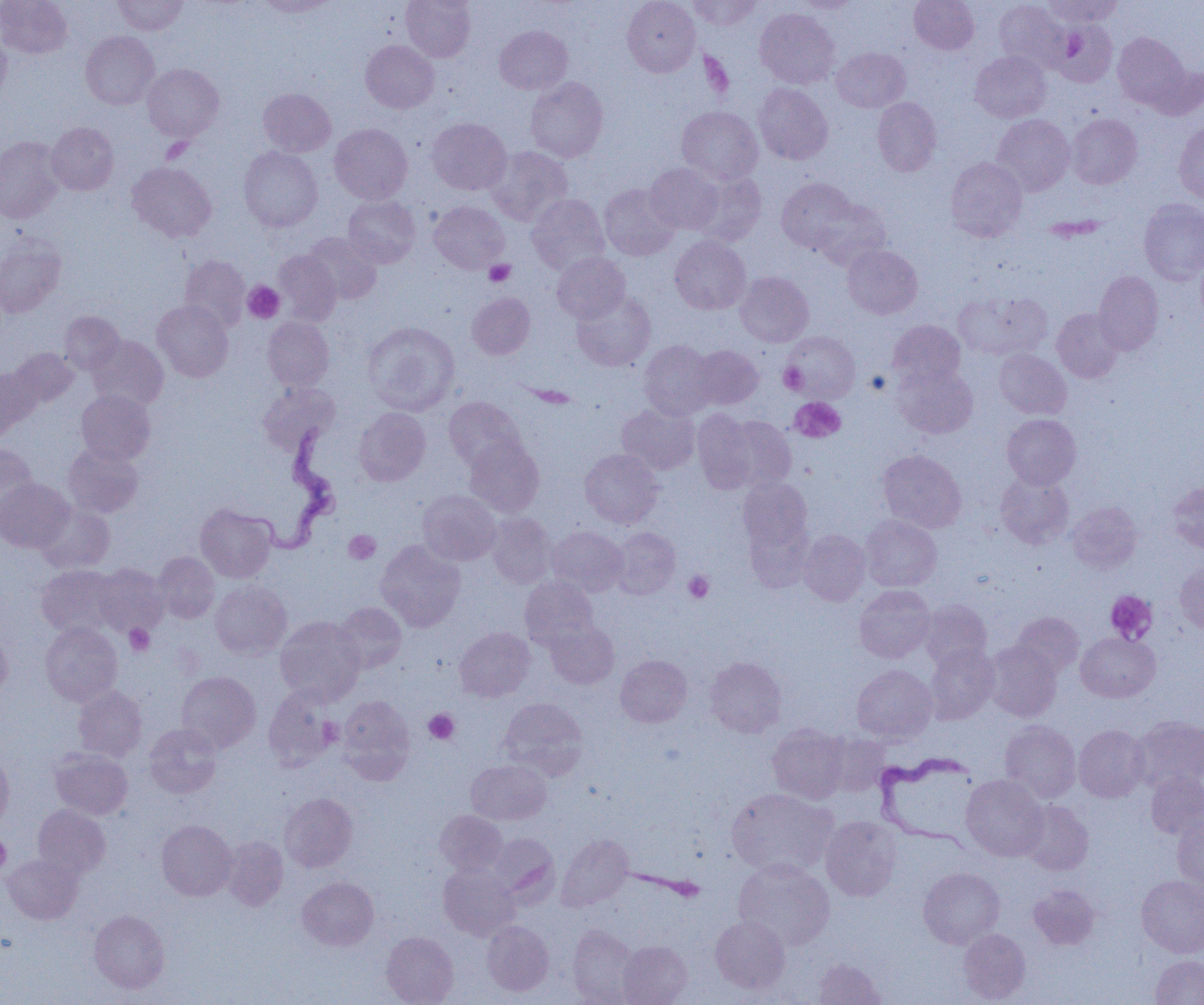

Summary:
  - Coordinate format: approximate bounding boxes as named x1/y1/x2/y2 corners in pixels
  - Trypanosoma brucei locations: (x1=244, y1=421, x2=342, y2=554), (x1=875, y1=750, x2=978, y2=850)
  - Platelet locations: (x1=161, y1=137, x2=192, y2=163), (x1=485, y1=259, x2=515, y2=286), (x1=243, y1=281, x2=284, y2=323), (x1=779, y1=363, x2=807, y2=394), (x1=865, y1=370, x2=890, y2=395), (x1=790, y1=397, x2=845, y2=442), (x1=344, y1=530, x2=381, y2=564), (x1=684, y1=571, x2=714, y2=603), (x1=1105, y1=590, x2=1157, y2=643), (x1=124, y1=624, x2=155, y2=655), (x1=424, y1=709, x2=459, y2=744), (x1=318, y1=717, x2=344, y2=746), (x1=0, y1=835, x2=10, y2=875)
  - Uninfected red blood cell locations: (x1=0, y1=0, x2=71, y2=58), (x1=112, y1=0, x2=188, y2=35), (x1=254, y1=0, x2=337, y2=17), (x1=401, y1=0, x2=475, y2=61), (x1=622, y1=0, x2=700, y2=76), (x1=687, y1=0, x2=762, y2=30), (x1=909, y1=0, x2=979, y2=54), (x1=1044, y1=0, x2=1123, y2=27), (x1=792, y1=1, x2=860, y2=14), (x1=994, y1=1, x2=1068, y2=70), (x1=755, y1=8, x2=839, y2=88), (x1=1051, y1=20, x2=1117, y2=87), (x1=494, y1=25, x2=572, y2=94), (x1=81, y1=31, x2=159, y2=109), (x1=1113, y1=33, x2=1189, y2=109), (x1=0, y1=34, x2=11, y2=103), (x1=361, y1=39, x2=439, y2=113), (x1=831, y1=47, x2=910, y2=113), (x1=971, y1=51, x2=1051, y2=122), (x1=142, y1=64, x2=223, y2=141), (x1=1147, y1=64, x2=1204, y2=120), (x1=526, y1=77, x2=608, y2=162), (x1=754, y1=83, x2=833, y2=164), (x1=258, y1=88, x2=335, y2=157), (x1=873, y1=97, x2=941, y2=176), (x1=677, y1=107, x2=763, y2=184), (x1=1067, y1=114, x2=1142, y2=189), (x1=992, y1=115, x2=1075, y2=195), (x1=426, y1=117, x2=511, y2=194), (x1=1174, y1=121, x2=1204, y2=205), (x1=47, y1=122, x2=118, y2=195), (x1=330, y1=123, x2=412, y2=204), (x1=0, y1=137, x2=64, y2=223), (x1=487, y1=146, x2=572, y2=226), (x1=238, y1=147, x2=322, y2=231), (x1=945, y1=157, x2=1027, y2=241), (x1=128, y1=163, x2=216, y2=242), (x1=645, y1=163, x2=724, y2=234), (x1=689, y1=171, x2=766, y2=245), (x1=777, y1=178, x2=857, y2=252), (x1=599, y1=184, x2=679, y2=261), (x1=527, y1=194, x2=610, y2=274), (x1=343, y1=195, x2=420, y2=268), (x1=1139, y1=198, x2=1204, y2=285), (x1=812, y1=199, x2=891, y2=271), (x1=429, y1=201, x2=509, y2=273), (x1=303, y1=232, x2=381, y2=304), (x1=0, y1=235, x2=65, y2=317), (x1=670, y1=235, x2=751, y2=314), (x1=842, y1=244, x2=922, y2=318), (x1=274, y1=250, x2=342, y2=325), (x1=1196, y1=252, x2=1204, y2=329), (x1=552, y1=253, x2=630, y2=323), (x1=179, y1=255, x2=249, y2=330), (x1=1093, y1=270, x2=1163, y2=355), (x1=736, y1=271, x2=813, y2=347), (x1=572, y1=290, x2=656, y2=371), (x1=953, y1=290, x2=1052, y2=361), (x1=467, y1=292, x2=535, y2=359), (x1=153, y1=300, x2=233, y2=381), (x1=1052, y1=308, x2=1123, y2=382), (x1=59, y1=311, x2=124, y2=374), (x1=263, y1=317, x2=334, y2=391), (x1=887, y1=319, x2=966, y2=389), (x1=363, y1=322, x2=460, y2=415), (x1=783, y1=331, x2=860, y2=402), (x1=87, y1=336, x2=168, y2=410), (x1=638, y1=340, x2=718, y2=420), (x1=690, y1=345, x2=763, y2=409), (x1=10, y1=348, x2=79, y2=407), (x1=994, y1=349, x2=1071, y2=419), (x1=894, y1=363, x2=978, y2=438), (x1=0, y1=367, x2=38, y2=438), (x1=258, y1=383, x2=339, y2=454), (x1=76, y1=390, x2=155, y2=465), (x1=444, y1=396, x2=525, y2=471), (x1=616, y1=403, x2=699, y2=475), (x1=354, y1=407, x2=431, y2=486), (x1=692, y1=409, x2=759, y2=493), (x1=1002, y1=414, x2=1081, y2=489), (x1=721, y1=415, x2=796, y2=492), (x1=464, y1=437, x2=544, y2=517), (x1=0, y1=444, x2=38, y2=521), (x1=63, y1=444, x2=143, y2=517), (x1=580, y1=449, x2=663, y2=528), (x1=878, y1=449, x2=966, y2=532), (x1=996, y1=473, x2=1074, y2=548), (x1=738, y1=478, x2=812, y2=556), (x1=0, y1=479, x2=75, y2=553), (x1=1167, y1=482, x2=1204, y2=552), (x1=418, y1=490, x2=501, y2=565), (x1=1067, y1=501, x2=1142, y2=573), (x1=37, y1=504, x2=114, y2=573), (x1=196, y1=504, x2=276, y2=582), (x1=486, y1=512, x2=556, y2=589), (x1=860, y1=515, x2=942, y2=591), (x1=742, y1=517, x2=813, y2=592), (x1=547, y1=526, x2=628, y2=596), (x1=610, y1=528, x2=681, y2=599), (x1=798, y1=529, x2=870, y2=605), (x1=376, y1=540, x2=465, y2=631), (x1=153, y1=551, x2=219, y2=623), (x1=1175, y1=560, x2=1204, y2=635), (x1=93, y1=563, x2=167, y2=636), (x1=37, y1=565, x2=119, y2=638), (x1=520, y1=576, x2=598, y2=650), (x1=210, y1=582, x2=291, y2=659), (x1=854, y1=585, x2=934, y2=663), (x1=919, y1=600, x2=991, y2=670), (x1=333, y1=602, x2=406, y2=674), (x1=1011, y1=612, x2=1083, y2=678), (x1=275, y1=616, x2=365, y2=705), (x1=546, y1=621, x2=619, y2=688), (x1=40, y1=623, x2=122, y2=705), (x1=455, y1=627, x2=535, y2=702), (x1=0, y1=628, x2=12, y2=700), (x1=1076, y1=632, x2=1160, y2=702), (x1=983, y1=641, x2=1062, y2=722), (x1=924, y1=646, x2=998, y2=724), (x1=616, y1=655, x2=692, y2=727), (x1=705, y1=656, x2=787, y2=737), (x1=852, y1=664, x2=937, y2=743), (x1=177, y1=671, x2=260, y2=753), (x1=73, y1=686, x2=147, y2=761), (x1=263, y1=688, x2=340, y2=772), (x1=338, y1=695, x2=415, y2=782), (x1=498, y1=697, x2=588, y2=779), (x1=1132, y1=716, x2=1204, y2=792), (x1=1000, y1=720, x2=1081, y2=803), (x1=144, y1=723, x2=221, y2=798), (x1=768, y1=723, x2=849, y2=804), (x1=1074, y1=725, x2=1149, y2=802), (x1=821, y1=732, x2=890, y2=796), (x1=50, y1=749, x2=133, y2=819), (x1=0, y1=751, x2=14, y2=832), (x1=466, y1=759, x2=551, y2=825), (x1=1146, y1=772, x2=1204, y2=839), (x1=961, y1=774, x2=1047, y2=861), (x1=727, y1=788, x2=837, y2=877), (x1=280, y1=793, x2=358, y2=872), (x1=1018, y1=800, x2=1093, y2=875), (x1=33, y1=804, x2=110, y2=879), (x1=435, y1=810, x2=506, y2=875), (x1=1173, y1=815, x2=1203, y2=891), (x1=821, y1=816, x2=902, y2=901), (x1=157, y1=820, x2=236, y2=901), (x1=488, y1=833, x2=558, y2=903), (x1=556, y1=834, x2=633, y2=911), (x1=221, y1=836, x2=288, y2=911), (x1=2, y1=853, x2=82, y2=923), (x1=734, y1=858, x2=834, y2=949), (x1=439, y1=863, x2=519, y2=940), (x1=918, y1=867, x2=1004, y2=948), (x1=1136, y1=875, x2=1204, y2=957), (x1=297, y1=876, x2=378, y2=950), (x1=1028, y1=885, x2=1101, y2=949), (x1=89, y1=909, x2=169, y2=993), (x1=710, y1=915, x2=790, y2=992), (x1=482, y1=920, x2=554, y2=996), (x1=567, y1=924, x2=639, y2=1003), (x1=958, y1=928, x2=1030, y2=1003), (x1=381, y1=932, x2=458, y2=1005), (x1=618, y1=940, x2=692, y2=1004), (x1=1150, y1=955, x2=1204, y2=1005), (x1=814, y1=958, x2=886, y2=1004)
  - Slide-level diagnosis: Trypanosoma brucei
  - Image size: 1204×1005 pixels
  - Magnification: 1000x
  - Field of view: one of a larger specimen
  - Modality: light microscopy
  - Preparation: thin blood film